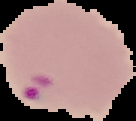

image size = 136×121 pixels
malaria status = parasitized
preparation = thin blood smear
image type = segmented cell region on a black background